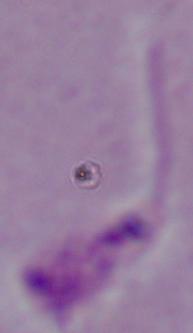 A Leishmania parasite is seen. 1000x magnification. Micrograph.